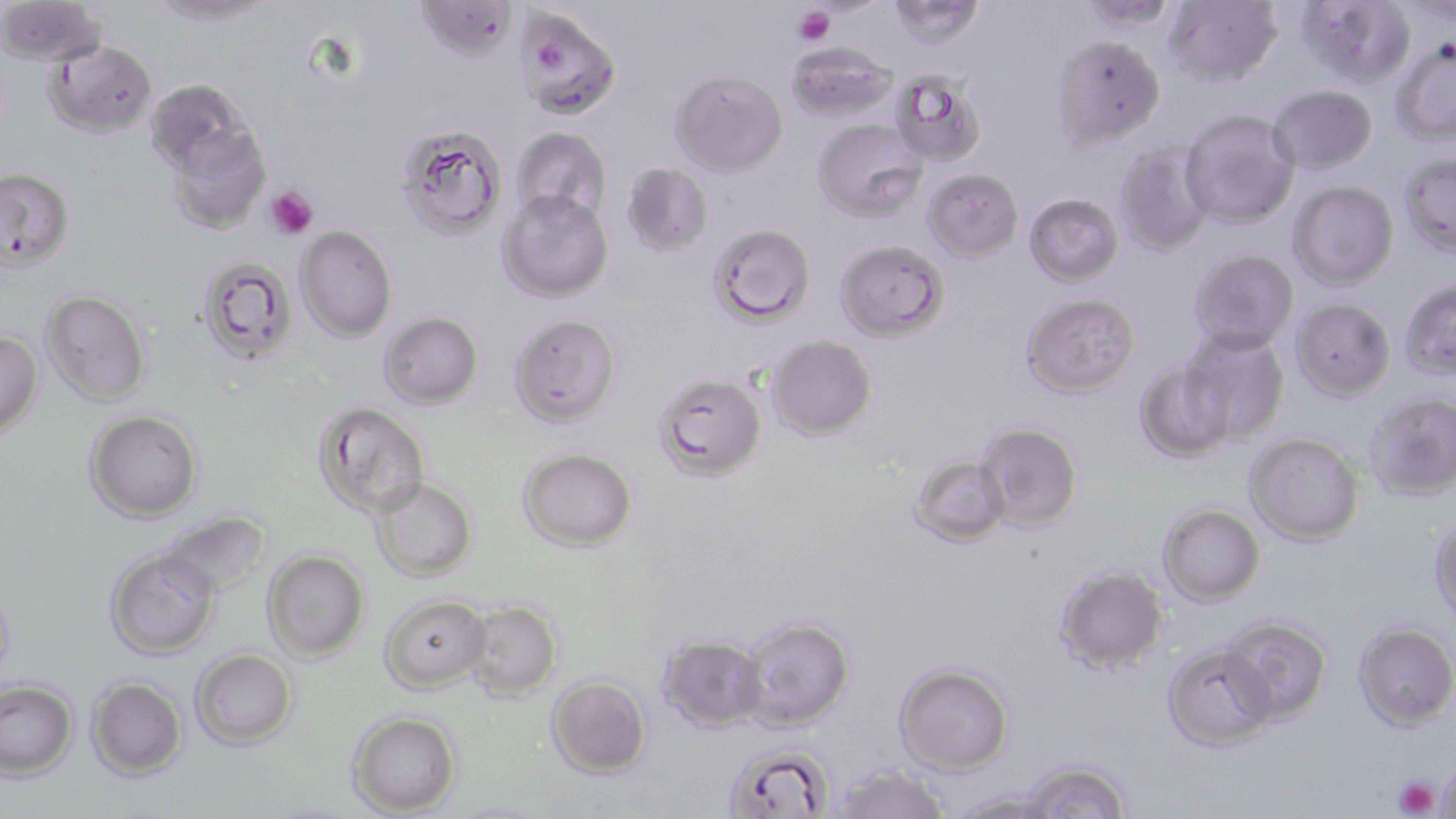

Summary:
  - Coordinate format: approximate bounding boxes as (x1, y1, x2, y2) in pixels
  - Uninfected red blood cell locations: (149, 0, 278, 27), (414, 0, 518, 62), (887, 0, 986, 48), (1078, 0, 1182, 30), (1163, 0, 1282, 87), (1296, 0, 1417, 88), (0, 1, 106, 68), (1394, 1, 1456, 25), (514, 7, 622, 121), (1052, 34, 1165, 149), (45, 39, 157, 138), (786, 40, 899, 123), (1391, 42, 1456, 146), (890, 68, 987, 167), (670, 69, 788, 177), (145, 78, 251, 177), (1268, 85, 1377, 174), (1179, 109, 1299, 228), (813, 118, 927, 221), (164, 122, 271, 234), (397, 124, 507, 241), (511, 126, 611, 225), (1115, 143, 1213, 255), (1399, 152, 1456, 258), (622, 163, 713, 256), (0, 166, 76, 269), (923, 168, 1024, 262), (1288, 180, 1399, 289), (497, 188, 613, 303), (1025, 193, 1123, 287), (708, 222, 816, 327), (295, 225, 397, 342), (835, 239, 949, 341), (1189, 249, 1299, 353), (197, 256, 297, 366), (1400, 279, 1456, 381), (41, 289, 151, 406), (1021, 293, 1140, 398), (1290, 297, 1396, 400), (379, 311, 483, 409), (509, 313, 621, 428), (0, 330, 43, 439), (1179, 330, 1290, 445), (766, 334, 877, 441), (1134, 361, 1234, 463), (653, 371, 767, 481), (1365, 392, 1456, 500), (314, 402, 431, 518), (85, 409, 203, 522), (976, 422, 1083, 531), (1245, 433, 1364, 545), (518, 447, 637, 551), (909, 454, 1012, 547), (370, 478, 478, 581), (1158, 504, 1265, 606), (160, 511, 270, 597), (1430, 516, 1456, 628), (105, 548, 221, 659), (262, 549, 370, 662), (1054, 564, 1168, 674), (0, 580, 17, 687), (380, 594, 492, 693), (463, 599, 562, 701), (738, 616, 855, 730), (1221, 617, 1332, 723), (1353, 622, 1456, 731), (657, 633, 768, 732), (1163, 644, 1277, 751), (190, 648, 298, 749), (894, 663, 1014, 774), (86, 675, 187, 779), (546, 675, 652, 778), (0, 679, 78, 779), (347, 710, 462, 817), (723, 743, 835, 818), (1019, 759, 1132, 819), (1438, 759, 1456, 819), (831, 764, 950, 819), (949, 791, 1064, 819), (443, 800, 555, 819)
  - Platelet locations: (794, 5, 835, 46), (540, 39, 570, 74), (265, 187, 318, 239), (1392, 774, 1442, 818)
  - Slide-level diagnosis: Plasmodium falciparum
  - Magnification: 1000x
  - Field of view: one of a larger specimen
  - Image size: 1456×819 pixels
  - Stain: May-Grünwald-Giemsa
  - Modality: light microscopy
  - Preparation: thin blood smear